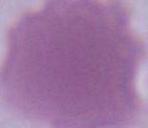

identification = erythrocyte
modality = micrograph
magnification = 1000x